Assess the morphology of the erythrocytes.
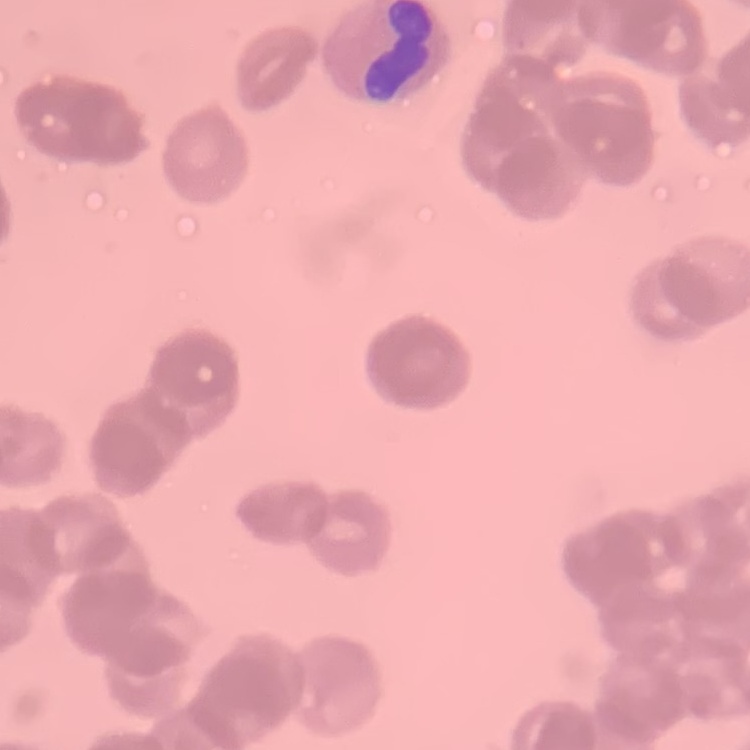
They show rouleaux formation.

Summary:
  - Stain: Field's or Giemsa
  - Image type: square crop of a larger photomicrograph
  - Preparation: thin blood film